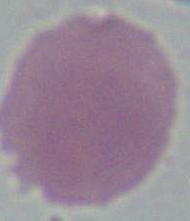
Summary:
  - Modality: micrograph
  - Magnification: 1000x
  - Identification: erythrocyte